Assess this cell for malaria.
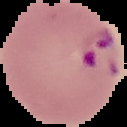
It is parasitized.

Image is 127×127 pixels. From a thin blood smear. The area outside the segmented cell region is set to black.